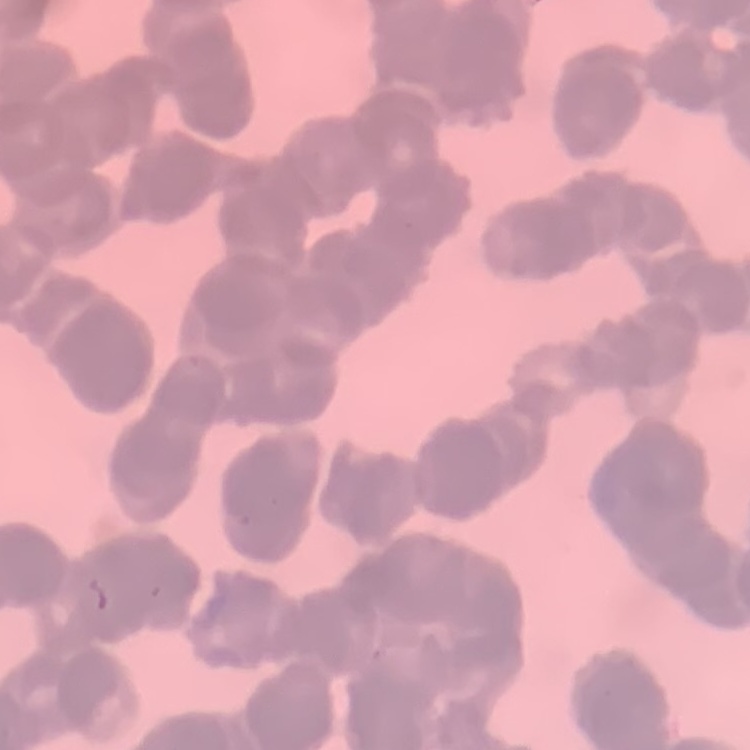
erythrocyte_morphology: rouleaux formation
preparation: thin blood film
stain: Field's or Giemsa
image_type: one tile cut from a larger photomicrograph